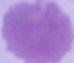 A red blood cell is shown. Captured at 1000x magnification. Micrograph.